Name the parasite shown.
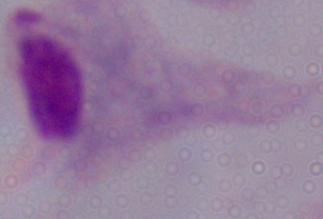
A trichomonad.

magnification: 1000x
modality: photomicrograph